Locate and identify every blood parasite.
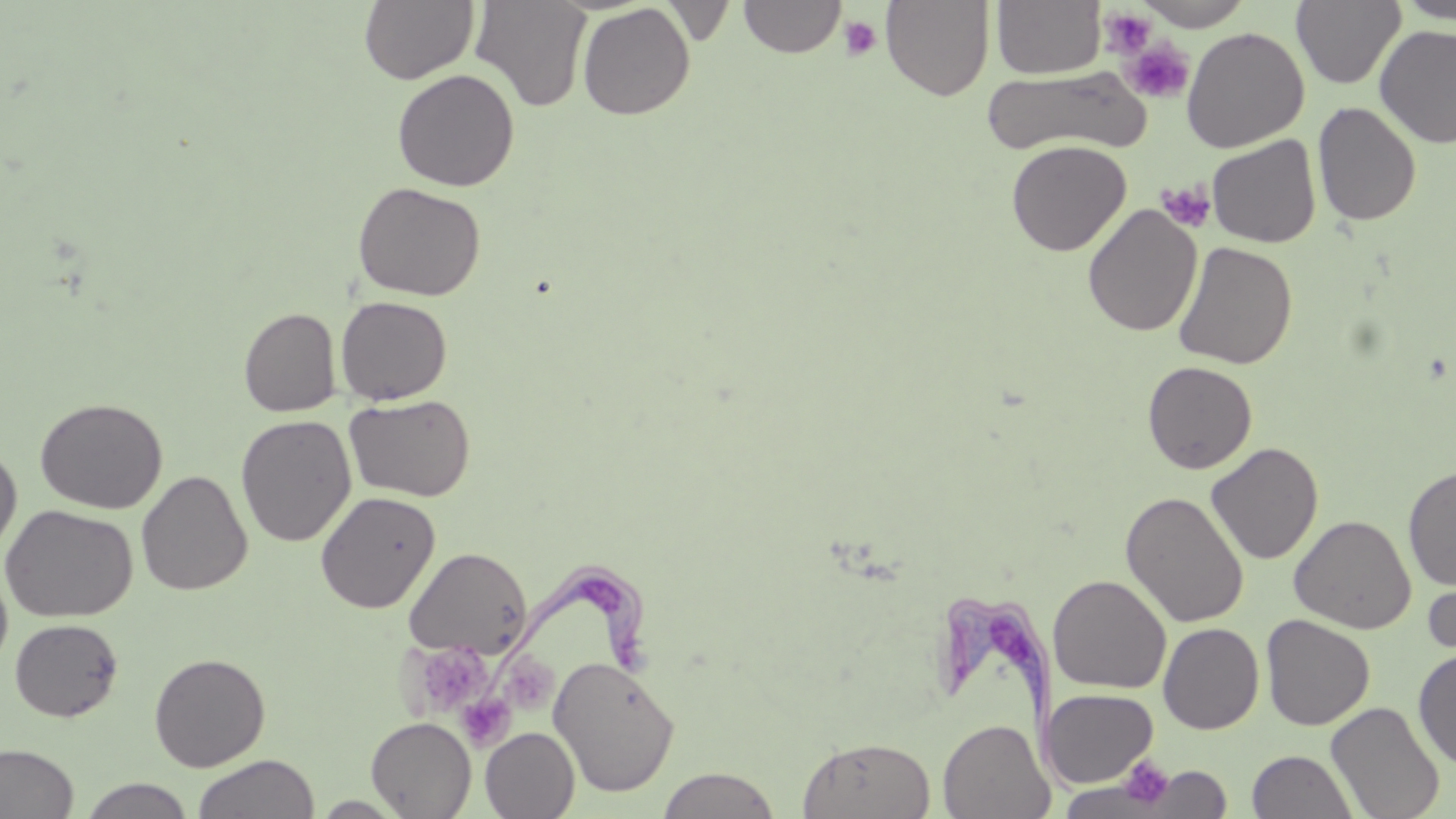

Approximate bounding boxes as (x1,y1)-(x2,y2) corner pairs in pixels.
Trypanosoma brucei: (482,558)-(659,684), (940,588)-(1082,795).
No Plasmodium falciparum, Plasmodium ovale, Plasmodium malariae, Plasmodium vivax, or Babesia divergens observed.

Summary:
  - Platelet locations: (1100,7)-(1158,58), (839,15)-(883,60), (1121,38)-(1195,104), (1156,181)-(1216,234), (410,640)-(492,715), (500,653)-(557,715), (456,692)-(515,750), (1117,756)-(1176,810)
  - Uninfected red blood cell locations: (359,0)-(479,84), (470,0)-(593,112), (739,0)-(845,58), (880,0)-(995,101), (992,0)-(1106,79), (1291,0)-(1406,89), (1395,0)-(1456,24), (1133,1)-(1254,30), (577,3)-(695,120), (1374,25)-(1456,148), (1181,26)-(1310,153), (983,66)-(1148,158), (392,68)-(520,191), (1312,102)-(1421,227), (1206,135)-(1321,248), (1006,140)-(1131,256), (352,181)-(486,301), (1082,203)-(1202,337), (1173,240)-(1297,369), (335,295)-(453,405), (238,307)-(341,417), (1142,361)-(1257,474), (344,393)-(476,502), (34,396)-(168,514), (235,414)-(357,547), (0,442)-(22,561), (1206,442)-(1324,564), (1403,466)-(1456,591), (136,470)-(252,596), (315,490)-(440,613), (1120,491)-(1250,628), (1,504)-(138,623), (1290,515)-(1416,633), (404,546)-(532,659), (1421,560)-(1456,667), (0,564)-(13,675), (1047,574)-(1171,694), (1261,615)-(1375,730), (10,618)-(124,722), (1158,623)-(1264,734), (1413,647)-(1456,770), (149,652)-(270,771), (549,655)-(679,796), (1041,688)-(1159,788), (1326,700)-(1445,819), (365,717)-(476,818), (937,718)-(1054,819), (480,727)-(579,818), (797,735)-(936,819), (0,743)-(79,819), (1247,749)-(1358,819), (193,754)-(319,819), (1128,764)-(1231,818), (656,767)-(782,819), (79,777)-(196,819), (309,795)-(410,817)
  - Slide-level diagnosis: Trypanosoma brucei
  - Field of view: single
  - Magnification: 1000x
  - Preparation: thin blood film
  - Image size: 1456×819 pixels
  - Stain: May-Grünwald-Giemsa
  - Modality: optical microscopy